Find the cells and give the type of each one.
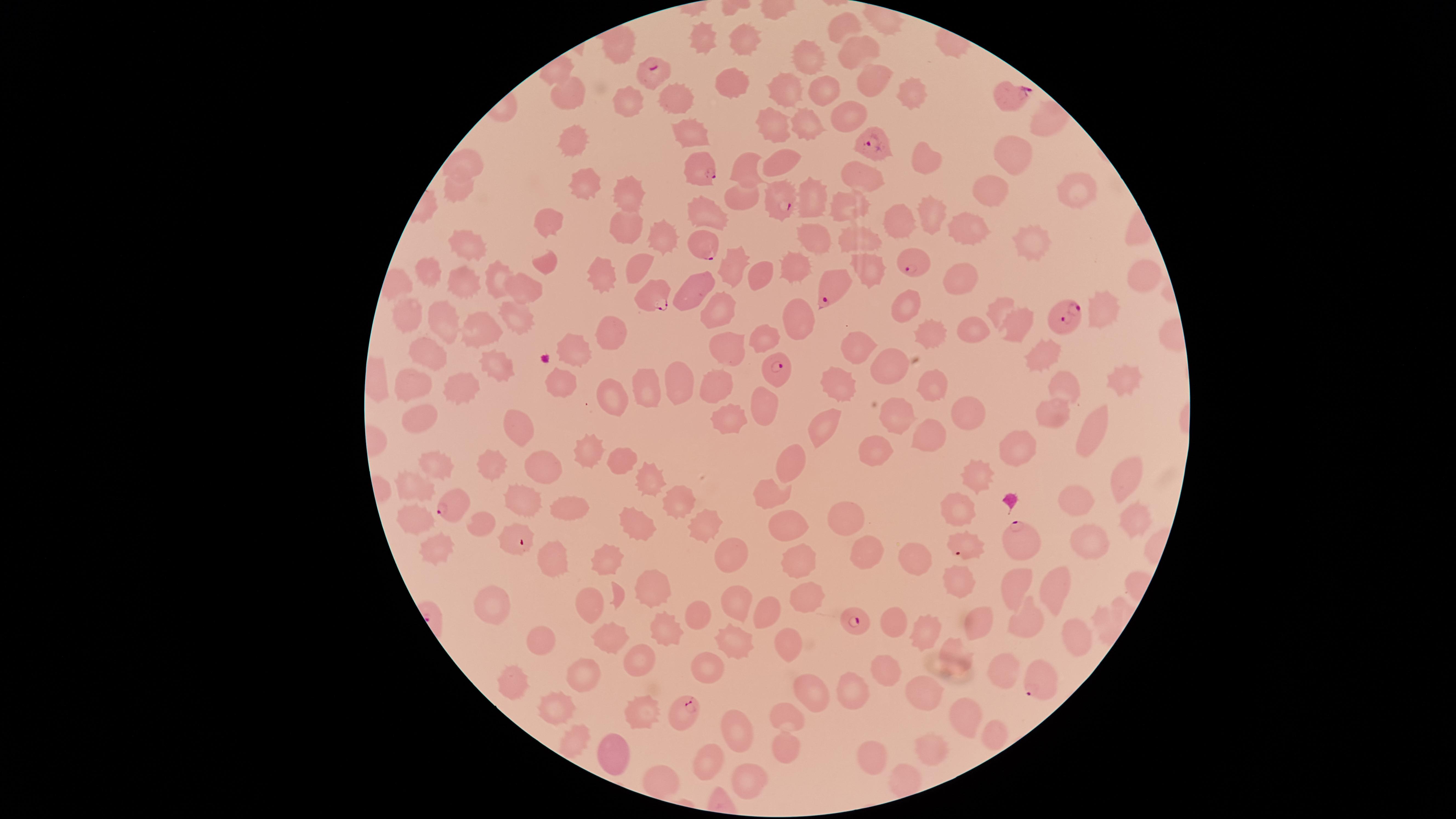

Approximate marker points as (x, y) in pixels.
Parasitized RBCs: (655, 70), (1008, 99), (870, 147), (703, 170), (781, 201), (705, 244), (915, 267), (835, 288), (653, 294), (1063, 316), (773, 365), (452, 506), (516, 541), (1021, 542), (959, 546), (856, 620), (1039, 679), (688, 713).
Uninfected RBCs: (847, 25), (703, 41), (741, 44), (862, 49), (619, 52), (807, 56), (873, 80), (732, 81), (821, 87), (787, 88), (909, 95), (571, 99), (676, 100), (629, 105), (850, 120), (811, 123), (1042, 126), (780, 127), (690, 133), (575, 143), (1015, 156), (926, 158), (471, 160), (784, 161), (745, 165), (863, 177), (582, 179), (1075, 189), (458, 191), (999, 194), (744, 195), (626, 196), (815, 202), (853, 205), (714, 209), (930, 215), (898, 219), (553, 225), (626, 225), (968, 232), (661, 237), (862, 238), (816, 241), (1032, 241), (469, 244), (639, 262), (548, 266), (732, 267), (866, 267), (431, 270), (801, 270), (760, 273), (968, 274), (498, 276), (1144, 276), (606, 279), (462, 280), (529, 288), (701, 289), (905, 305), (1003, 308), (1102, 309), (727, 310), (408, 314), (516, 316), (803, 320), (446, 323), (1017, 325), (935, 326), (978, 328), (614, 329), (473, 331), (765, 340), (859, 349), (727, 351), (430, 352), (1047, 353), (579, 354), (498, 367), (892, 369), (843, 375), (564, 378), (678, 378), (1067, 378), (1119, 378), (647, 379), (723, 382), (409, 383), (934, 383), (465, 385), (612, 390), (758, 402), (1052, 410), (970, 411), (903, 415), (733, 416), (829, 421), (421, 422), (1090, 428), (930, 431), (517, 438), (1021, 449), (876, 451), (592, 454), (620, 458), (436, 464), (548, 466), (790, 468), (492, 472), (981, 476), (1124, 482), (650, 484), (416, 488), (774, 493), (523, 498), (684, 499), (1075, 502), (963, 507), (571, 510), (848, 519), (1128, 520), (417, 522), (481, 522), (633, 525), (788, 525), (704, 530), (1092, 543), (439, 545), (864, 555), (731, 556), (612, 559), (556, 561), (916, 562), (799, 565), (1016, 584), (1057, 586), (967, 587), (650, 588), (808, 599), (736, 602), (588, 604), (490, 605), (768, 611), (701, 613), (1025, 616), (894, 621), (982, 621), (921, 626), (1073, 630), (664, 631), (543, 640), (610, 642), (733, 642), (787, 642), (957, 654), (641, 663), (884, 668), (1000, 669), (707, 670), (586, 674), (514, 682), (924, 689), (810, 691), (859, 691), (564, 703), (639, 708), (793, 713), (968, 714), (735, 727), (997, 734), (576, 739), (785, 746), (927, 746), (609, 757), (873, 757), (706, 760), (658, 780), (746, 784).
No WBCs identified.

visible region = circular
preparation = thin smear of blood
field of view = single
stain = Giemsa
image size = 1456×819 pixels
capture = smartphone photograph through the microscope eyepiece
species = Plasmodium falciparum